Describe the morphology of the erythrocytes.
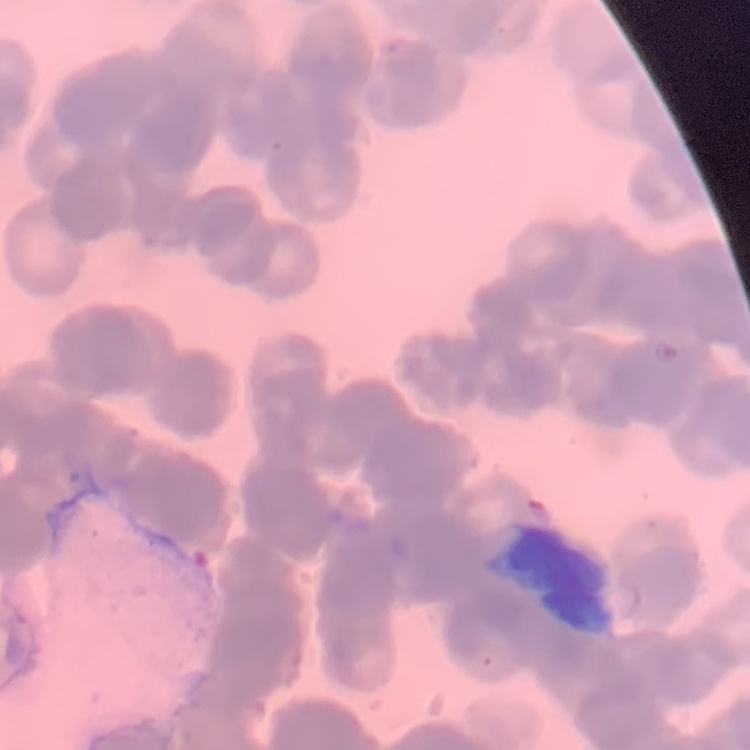

They show rouleaux formation.

preparation = thin peripheral smear
stain = Field's or Giemsa
image type = one tile cut from a larger photomicrograph